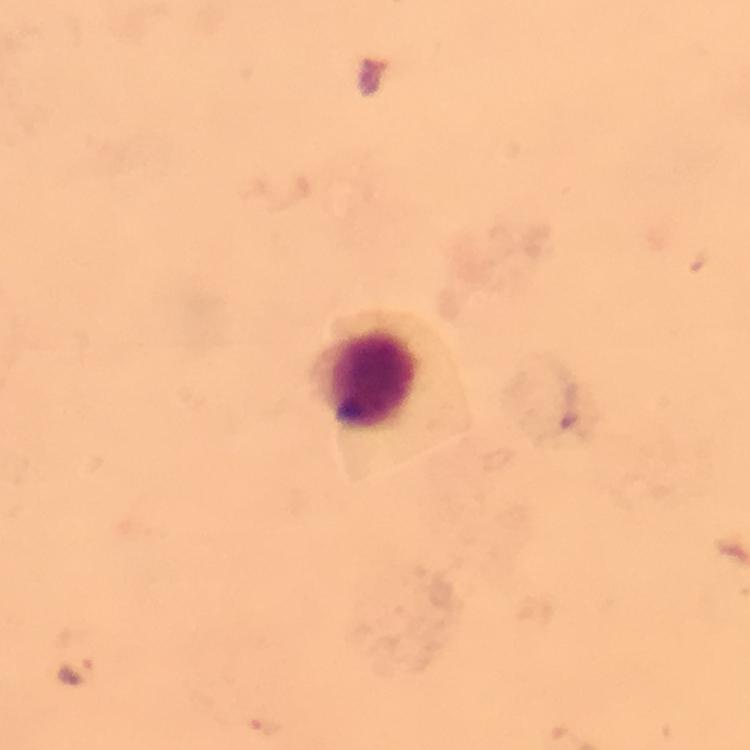 Approximate centers as [x, y] in pixels. Malaria parasite locations: [561, 389], [75, 672], [262, 727]. Leukocyte locations: [376, 384]. A crop from one field of view. Photographed with a smartphone mounted on the microscope. From a malaria diagnostic workup. Immersion oil was used. Thick smear. At 100x magnification. Giemsa stain. Image is 750×750 pixels.